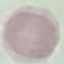 Result: no malaria parasites detected. Giemsa stain. Acquired by smartphone through the microscope eyepiece. Cell patch, automatically extracted from a larger field of view and resized to 64 × 64 pixels. Thin blood smear.